Classify this cell by malaria status.
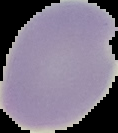

Parasitized.

Summary:
  - Image size: 118×133 pixels
  - Image type: segmented cell region on a black background
  - Preparation: thin blood film